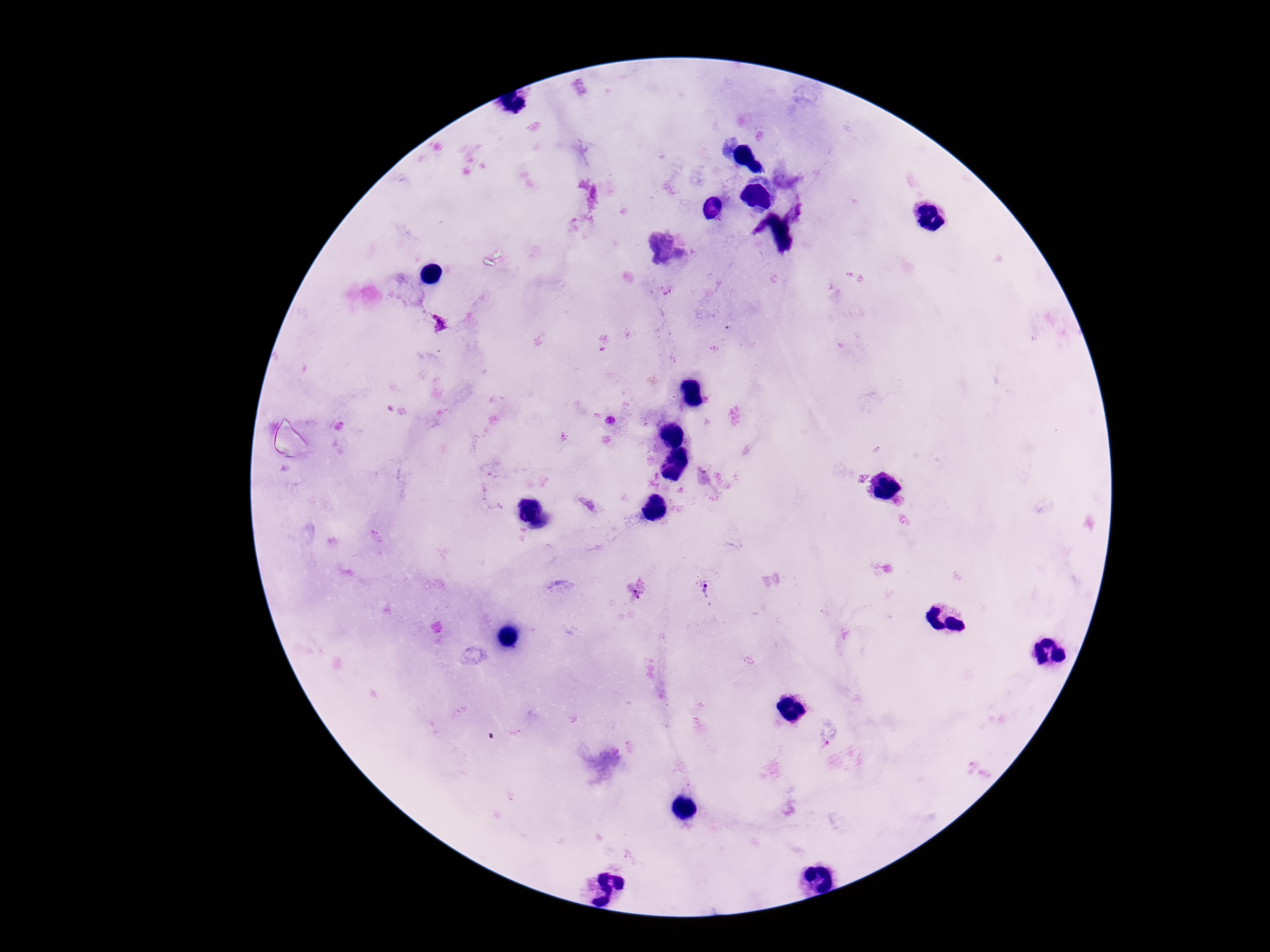

Approximate centers as {x, y} in pixels.
Summary:
  - Plasmodium parasite locations: {440, 324}, {636, 591}, {708, 592}
  - Field of view: one from this slide
  - Patient malaria status: infected
  - Image size: 1270×952 pixels
  - Capture: smartphone camera through the microscope eyepiece
  - Preparation: thick blood smear
  - Magnification: 100x
  - Stain: Giemsa